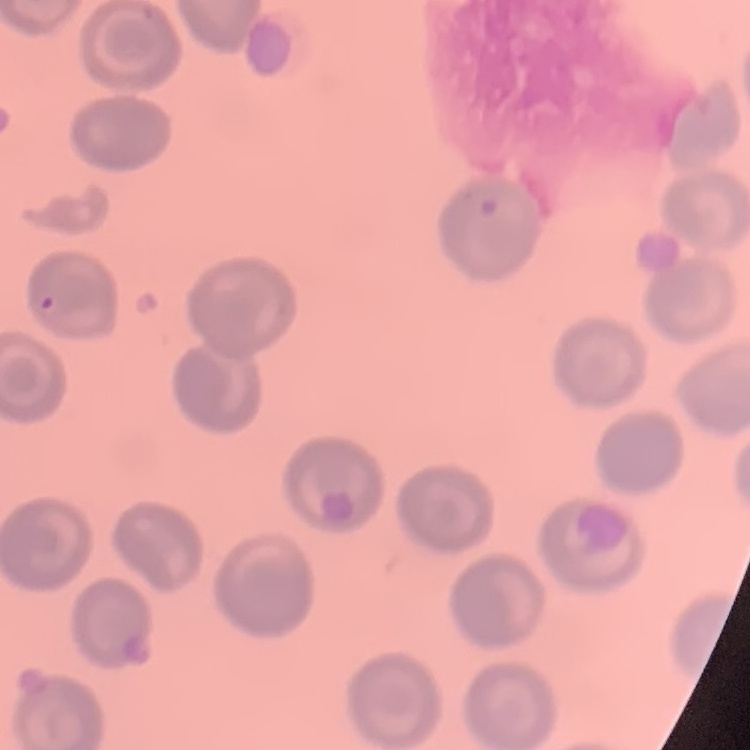
Summary:
  - Erythrocyte morphology: no rouleaux formation
  - Image type: square crop of a larger photomicrograph
  - Preparation: thin blood smear
  - Stain: Field's or Giemsa